Report the malaria status of this cell.
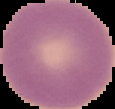
Uninfected.

preparation = thin blood smear
image size = 115×109 pixels
image type = segmented cell region with the area outside set to black